Describe the morphology of the red blood cells.
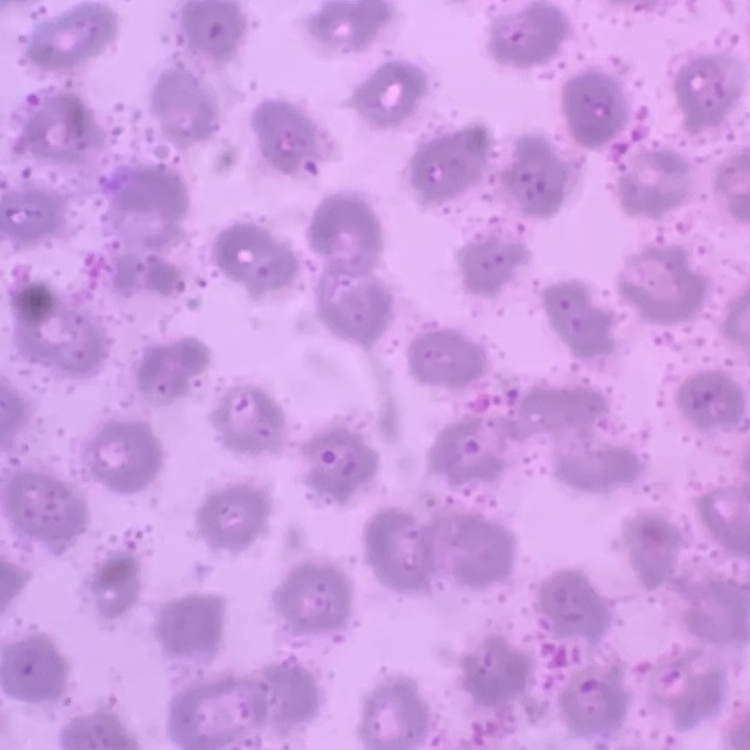

They show no rouleaux formation.

Summary:
  - Stain: Field's or Giemsa
  - Preparation: thin blood film
  - Image type: one tile cut from a larger photomicrograph